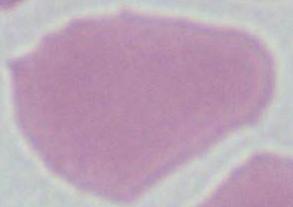

Summary:
  - Magnification: 1000x
  - Identification: erythrocyte
  - Modality: micrograph